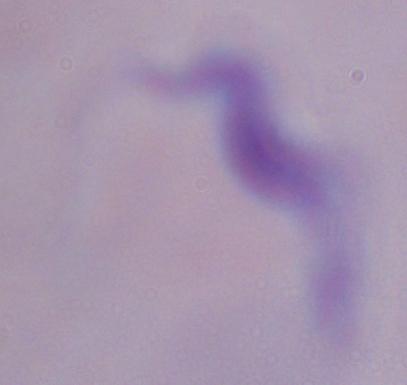
identification = trypanosome
modality = photomicrograph
magnification = 1000x